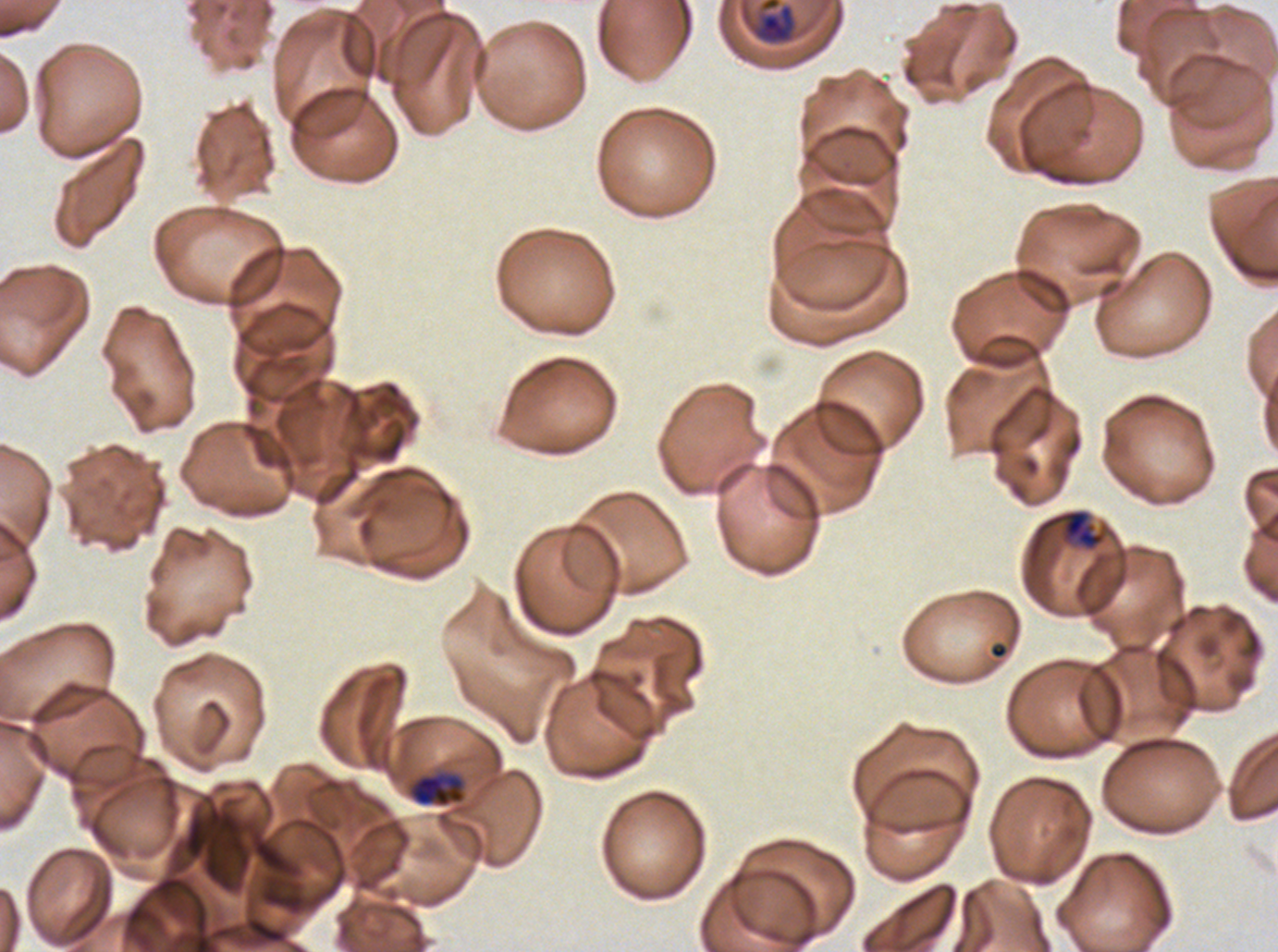

Approximate bounding boxes as (x1, y1, x2, y2) in pixels.
Summary:
  - Late-ring/early-trophozoite locations: (1063, 509, 1105, 549), (408, 772, 466, 808)
  - Mid trophozoite locations: (750, 0, 797, 45)
  - Stain: Giemsa
  - Image size: 1278×952 pixels
  - Preparation: thin blood smear
  - Field of view: one sub-image of a larger composite
  - Life-cycle stages observed: late-ring/early-trophozoite, mid trophozoite
  - Specimen: ex-vivo P. falciparum culture from a patient in The Gambia, grown for 24 to 48 hours